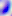
modality = photomicrograph
identification = Toxoplasma gondii
magnification = 400x